Give the extent of all Plasmodium falciparum-infected red blood cells.
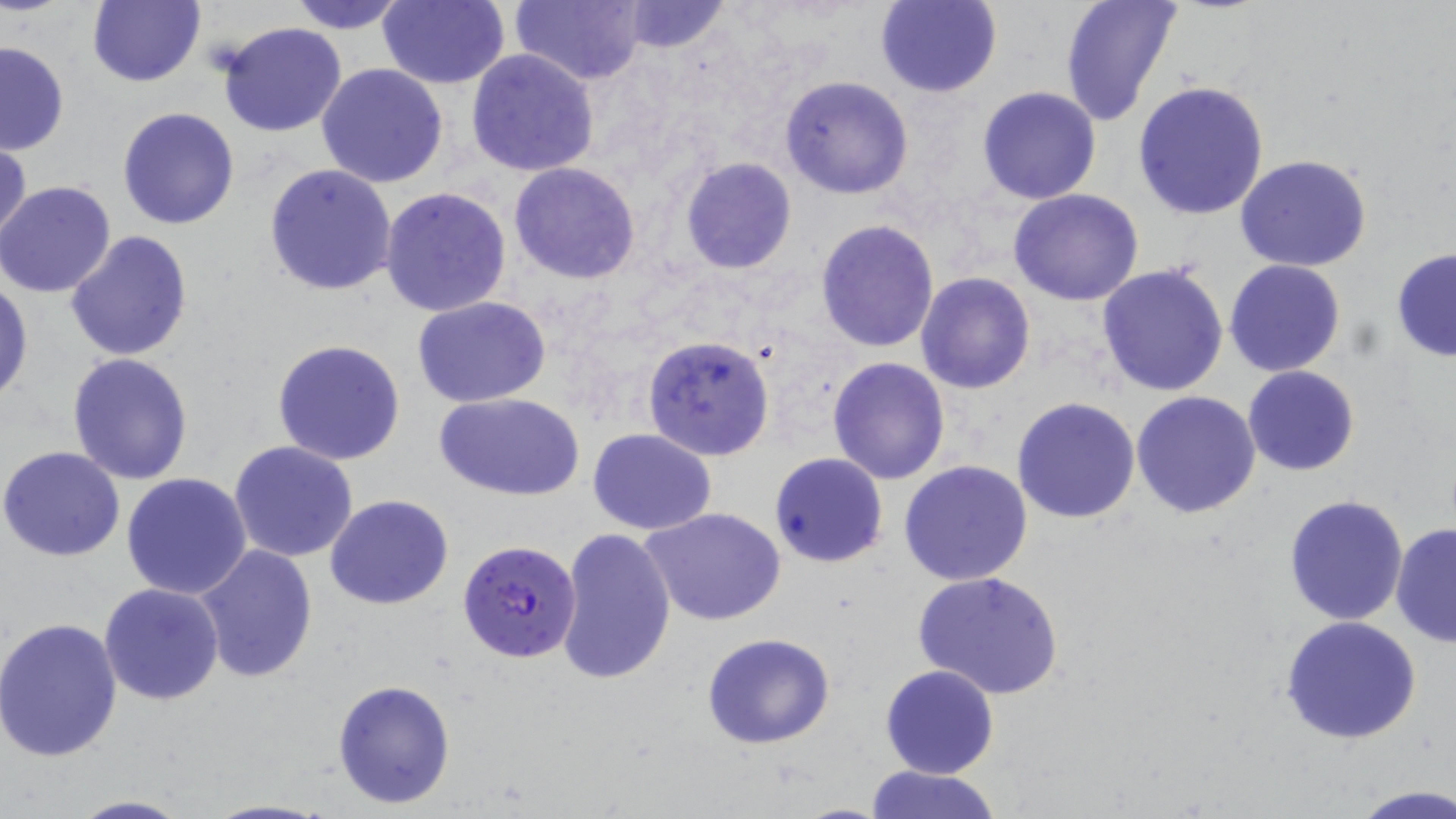

Approximate bounding boxes as named x1/y1/x2/y2 corners in pixels.
Plasmodium falciparum-infected red blood cells: (x1=457, y1=539, x2=582, y2=663).

Summary:
  - Uninfected red blood cell locations: (x1=87, y1=0, x2=205, y2=89), (x1=287, y1=0, x2=410, y2=34), (x1=378, y1=0, x2=511, y2=89), (x1=508, y1=0, x2=648, y2=86), (x1=874, y1=0, x2=1003, y2=98), (x1=1060, y1=0, x2=1183, y2=125), (x1=616, y1=1, x2=732, y2=54), (x1=216, y1=21, x2=347, y2=137), (x1=0, y1=41, x2=70, y2=156), (x1=466, y1=48, x2=600, y2=176), (x1=317, y1=63, x2=449, y2=188), (x1=779, y1=75, x2=915, y2=200), (x1=1132, y1=81, x2=1272, y2=220), (x1=977, y1=85, x2=1103, y2=205), (x1=116, y1=107, x2=240, y2=230), (x1=0, y1=134, x2=30, y2=250), (x1=1234, y1=154, x2=1374, y2=273), (x1=679, y1=156, x2=798, y2=274), (x1=509, y1=162, x2=640, y2=283), (x1=263, y1=164, x2=398, y2=297), (x1=0, y1=179, x2=119, y2=298), (x1=381, y1=187, x2=512, y2=318), (x1=1007, y1=188, x2=1145, y2=306), (x1=815, y1=218, x2=940, y2=353), (x1=66, y1=230, x2=193, y2=362), (x1=1390, y1=247, x2=1456, y2=362), (x1=1224, y1=260, x2=1346, y2=377), (x1=1096, y1=263, x2=1231, y2=397), (x1=916, y1=272, x2=1035, y2=394), (x1=0, y1=278, x2=32, y2=405), (x1=411, y1=296, x2=553, y2=406), (x1=642, y1=334, x2=775, y2=461), (x1=272, y1=338, x2=406, y2=465), (x1=67, y1=352, x2=196, y2=485), (x1=827, y1=357, x2=950, y2=485), (x1=1242, y1=364, x2=1359, y2=476), (x1=1131, y1=391, x2=1262, y2=518), (x1=436, y1=392, x2=584, y2=500), (x1=1012, y1=396, x2=1142, y2=524), (x1=588, y1=427, x2=716, y2=534), (x1=229, y1=441, x2=359, y2=562), (x1=1, y1=446, x2=127, y2=562), (x1=769, y1=452, x2=888, y2=568), (x1=900, y1=460, x2=1033, y2=586), (x1=121, y1=473, x2=252, y2=599), (x1=325, y1=494, x2=453, y2=609), (x1=1281, y1=494, x2=1410, y2=627), (x1=642, y1=507, x2=787, y2=626), (x1=1390, y1=522, x2=1455, y2=648), (x1=555, y1=527, x2=677, y2=686), (x1=193, y1=545, x2=318, y2=686), (x1=913, y1=569, x2=1065, y2=701), (x1=100, y1=582, x2=224, y2=705), (x1=5, y1=598, x2=213, y2=734), (x1=1280, y1=615, x2=1423, y2=744), (x1=0, y1=616, x2=124, y2=762), (x1=701, y1=633, x2=836, y2=749), (x1=880, y1=664, x2=1000, y2=780), (x1=332, y1=679, x2=455, y2=810), (x1=862, y1=764, x2=1004, y2=819), (x1=1348, y1=784, x2=1456, y2=819), (x1=68, y1=795, x2=194, y2=819), (x1=203, y1=798, x2=334, y2=818)
  - Slide-level diagnosis: Plasmodium falciparum
  - Preparation: thin blood smear
  - Field of view: single
  - Magnification: 1000x
  - Modality: light microscopy
  - Image size: 1456×819 pixels
  - Stain: May-Grünwald-Giemsa